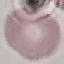

Summary:
  - Malaria status: uninfected
  - Preparation: thin blood film
  - Capture: smartphone camera at the microscope eyepiece
  - Stain: Giemsa
  - Image type: cell patch, automatically extracted from a larger field of view and resized to 64 × 64 pixels